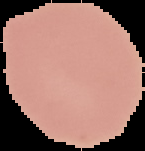

Summary:
  - Preparation: thin blood film
  - Image size: 145×151 pixels
  - Result: no Plasmodium parasites seen
  - Image type: segmented cell region with the area outside set to black